Assess the morphology of the erythrocytes.
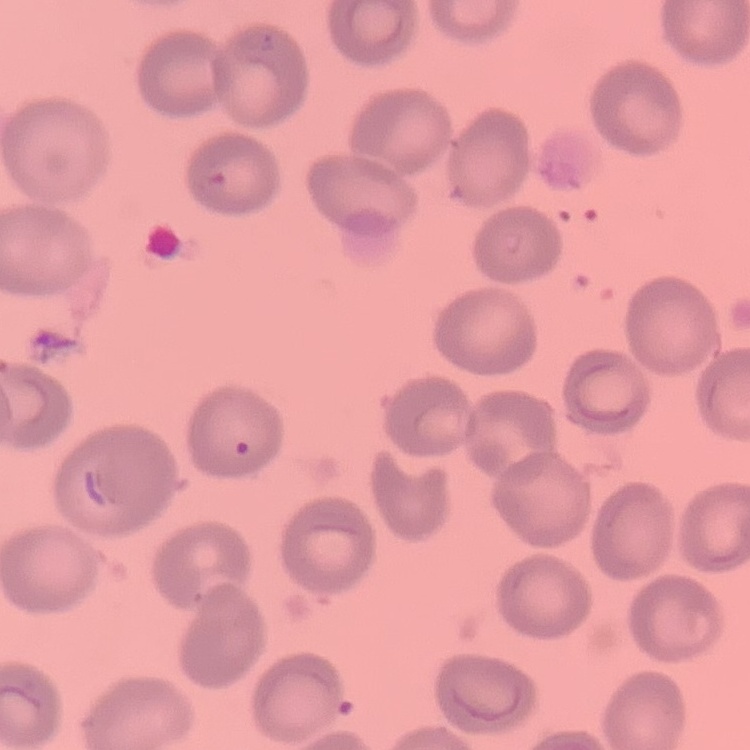

No rouleaux formation.

Stained with either Field's or Giemsa. Thin blood film. One tile cut from a larger photomicrograph.